Assess this cell for malaria.
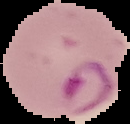

Parasitized.

Summary:
  - Image size: 130×124 pixels
  - Image type: segmented cell region with the area outside set to black
  - Preparation: thin blood film